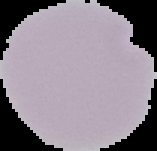
image_type: segmented cell region with the area outside set to black
preparation: thin blood film
result: negative for Plasmodium parasites
image_size: 157×151 pixels